Comment on the morphology of the red blood cells.
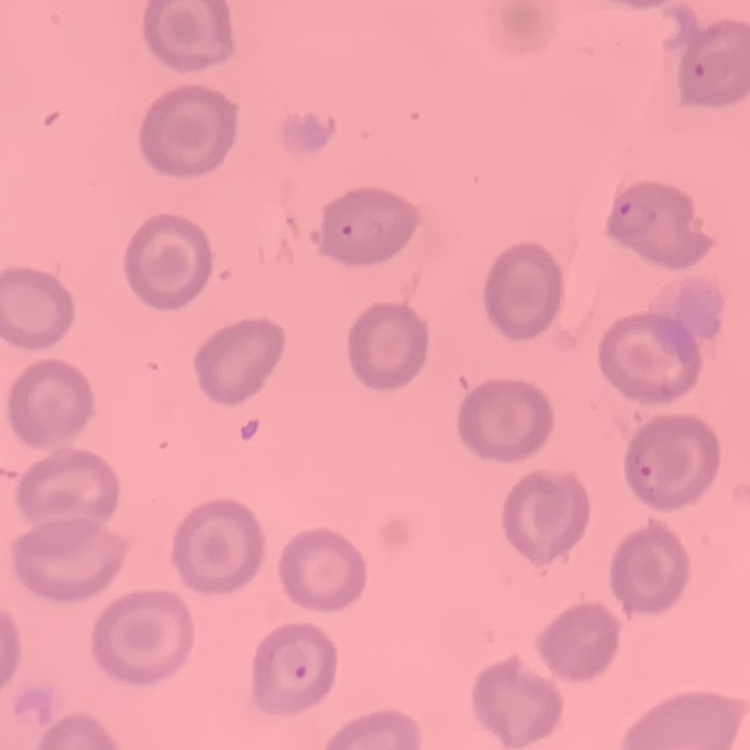

No rouleaux formation.

stain = Field's or Giemsa
image type = one tile cut from a larger photomicrograph
preparation = thin blood film